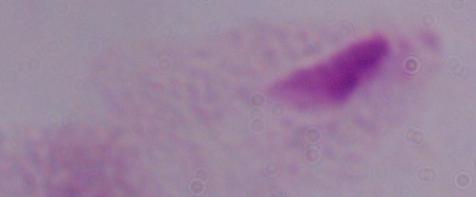
Photomicrograph. 1000x magnification. A trichomonad is shown.